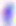
{
  "identification": "Toxoplasma gondii",
  "magnification": "400x",
  "modality": "photomicrograph"
}